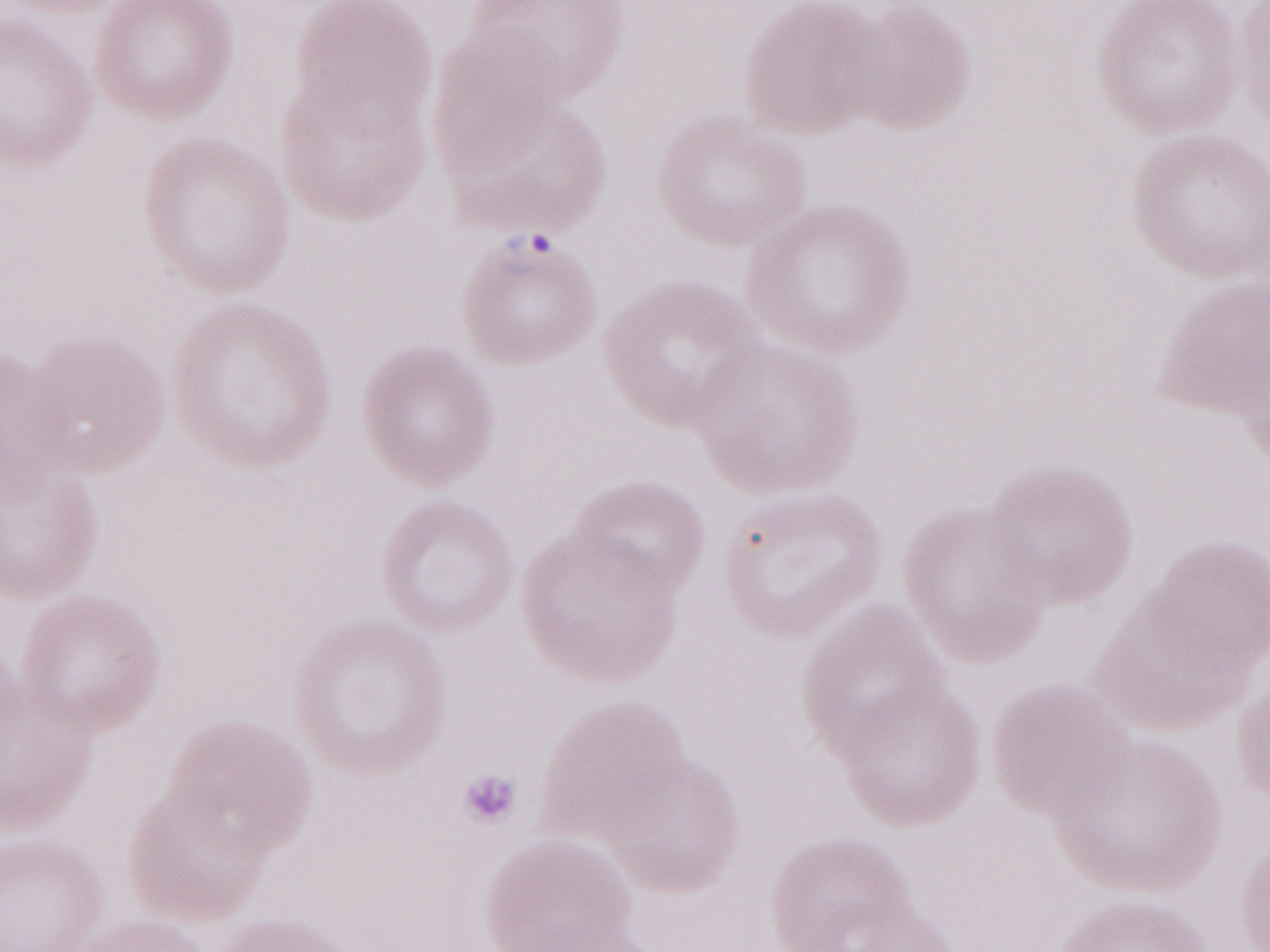
Patient diagnosis: malaria infection. Image is 1270×952 pixels. May-Grünwald-Giemsa-stained preparation. Thin blood smear. One field of this slide. Magnification: 1,000x. Olympus BX43 microscope and DP73 digital camera.